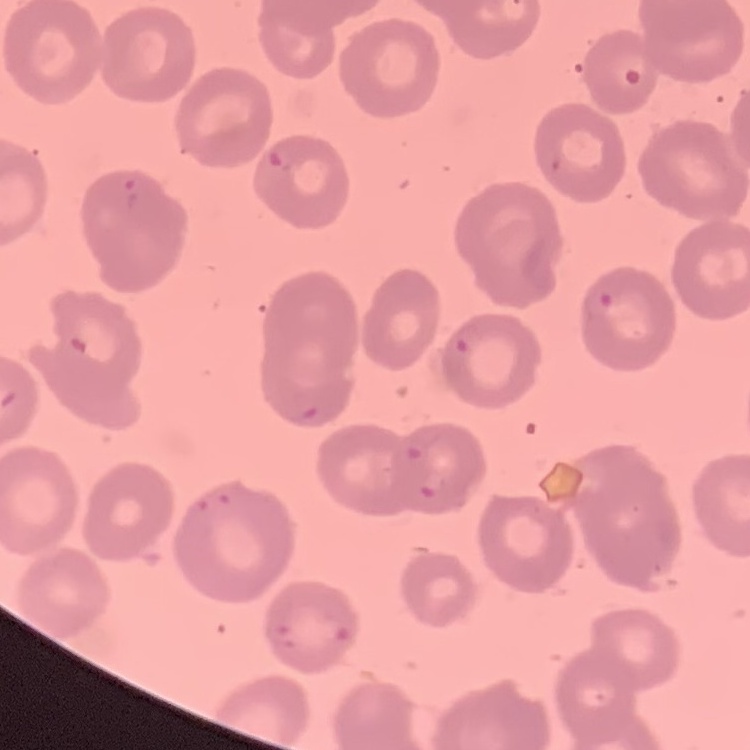

{
  "red_blood_cell_morphology": "no rouleaux formation",
  "image_type": "square crop of a larger photomicrograph",
  "stain": "Field's or Giemsa",
  "preparation": "thin peripheral smear"
}